Assess this cell for malaria.
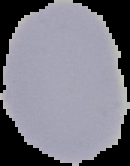
It is uninfected.

From a thin blood smear. Image is 130×166 pixels. Segmented cell region on a black background.